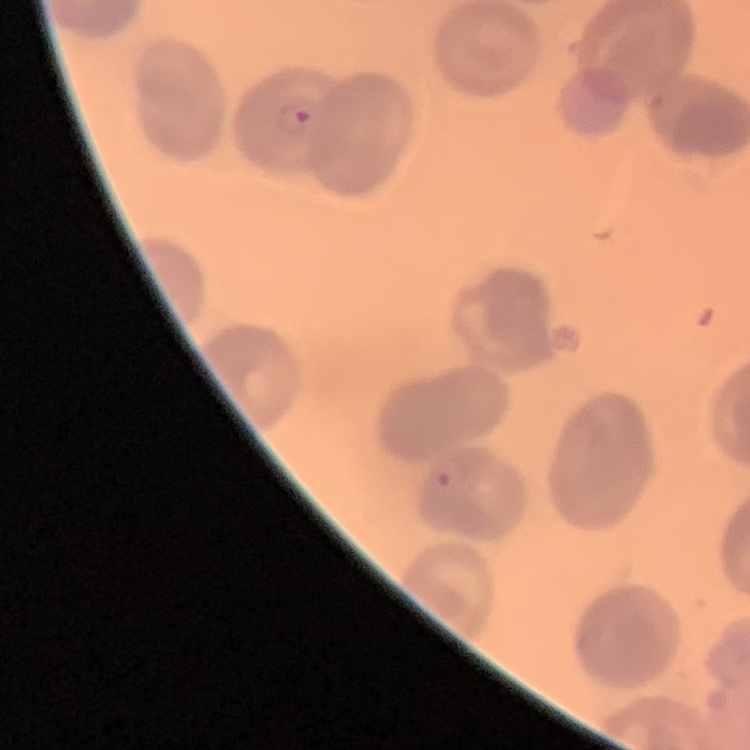

Summary:
  - Erythrocyte morphology: no rouleaux formation
  - Stain: Field's or Giemsa
  - Image type: one tile cut from a larger photomicrograph
  - Preparation: thin blood smear